Give the position of every malaria parasite and every leukocyte.
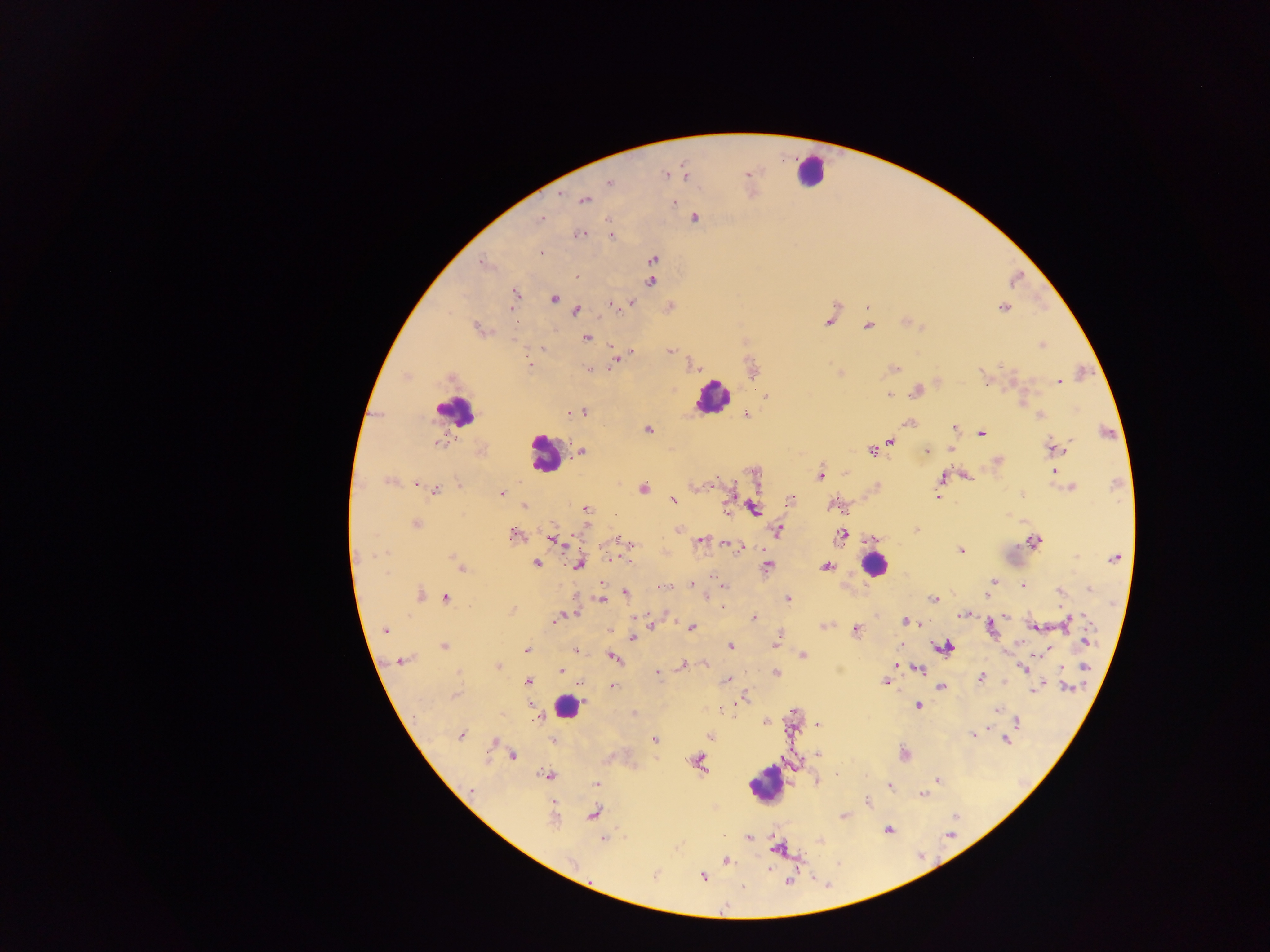
Approximate centers as [x, y] in pixels.
Malaria parasites: [665, 174], [748, 174], [686, 175], [609, 182], [585, 200], [673, 203], [696, 218], [541, 219], [607, 221], [581, 234], [612, 236], [541, 253], [653, 259], [483, 263], [576, 276], [651, 281], [514, 295], [553, 298], [631, 304], [612, 306], [622, 306], [511, 308], [868, 308], [1002, 308], [577, 310], [829, 321], [868, 327], [478, 329], [585, 338], [1043, 345], [543, 349], [670, 351], [629, 354], [617, 359], [527, 364], [892, 368], [752, 369], [588, 370], [1058, 381], [917, 391], [889, 395], [765, 396], [582, 412], [570, 413], [747, 414], [1040, 416], [908, 422], [955, 428], [647, 430], [982, 434], [891, 442], [439, 443], [1056, 448], [950, 449], [873, 450], [582, 451], [926, 451], [997, 462], [1054, 472], [756, 474], [820, 475], [967, 477], [942, 478], [389, 482], [458, 484], [415, 485], [710, 486], [940, 486], [1071, 487], [643, 489], [435, 491], [502, 492], [1020, 495], [938, 497], [791, 499], [673, 500], [831, 505], [524, 506], [754, 508], [586, 509], [416, 524], [678, 529], [916, 530], [777, 531], [513, 534], [841, 535], [553, 539], [700, 540], [624, 541], [1033, 541], [732, 546], [962, 551], [452, 557], [611, 558], [1114, 558], [536, 562], [579, 564], [767, 566], [826, 566], [462, 569], [992, 582], [692, 585], [1023, 585], [663, 587], [1090, 588], [1060, 591], [625, 593], [420, 594], [986, 594], [706, 597], [445, 598], [933, 599], [601, 600], [788, 600], [721, 607], [512, 610], [963, 615], [1006, 616], [754, 617], [558, 618], [1070, 620], [906, 621], [651, 625], [824, 625], [1034, 626], [990, 627], [691, 628], [385, 630], [855, 630], [632, 638], [1086, 641], [777, 642], [731, 645], [444, 647], [945, 648], [526, 650], [576, 650], [1036, 654], [803, 655], [614, 657], [402, 660], [683, 665], [497, 666], [917, 668], [1024, 668], [1085, 668], [561, 670], [657, 673], [775, 673], [980, 678], [728, 680], [528, 682], [581, 682], [886, 682], [612, 686], [942, 687], [1068, 687], [1036, 689], [744, 696], [918, 706], [997, 710], [539, 717], [766, 722], [1018, 722], [819, 724], [973, 735], [461, 736], [710, 736], [552, 740], [654, 740], [1006, 740], [818, 754], [904, 754], [513, 755], [699, 762], [548, 776], [937, 780], [597, 784], [890, 786], [922, 794], [868, 803], [594, 814], [843, 816], [552, 820], [888, 830], [749, 838], [603, 839], [821, 841], [778, 848], [727, 861], [768, 870], [702, 876], [788, 881].
Leukocytes: [810, 171], [712, 396], [456, 409], [545, 454], [874, 566], [566, 706], [768, 781].

Image is 1270×952 pixels. Single field of view. Thick blood smear. Sample from Ghana. Photographed through a microscope with a mobile-phone camera.